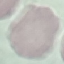
Malaria status: uninfected. Thin blood film. Acquired by smartphone through the microscope eyepiece. Giemsa-stained preparation. Automatically extracted cell patch, resized to 64 × 64 pixels.